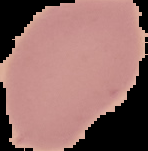 From a thin blood film. Image is 148×151 pixels. The area outside the segmented cell region is set to black. Result: no malaria parasites seen.